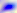
Summary:
  - Modality: photomicrograph
  - Magnification: 400x
  - Identification: Toxoplasma gondii